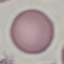

result = negative for malaria parasites
image type = automatically extracted cell patch, resized to 64 × 64 pixels
preparation = thin smear
stain = Giemsa
capture = smartphone through the microscope eyepiece